Locate platelets.
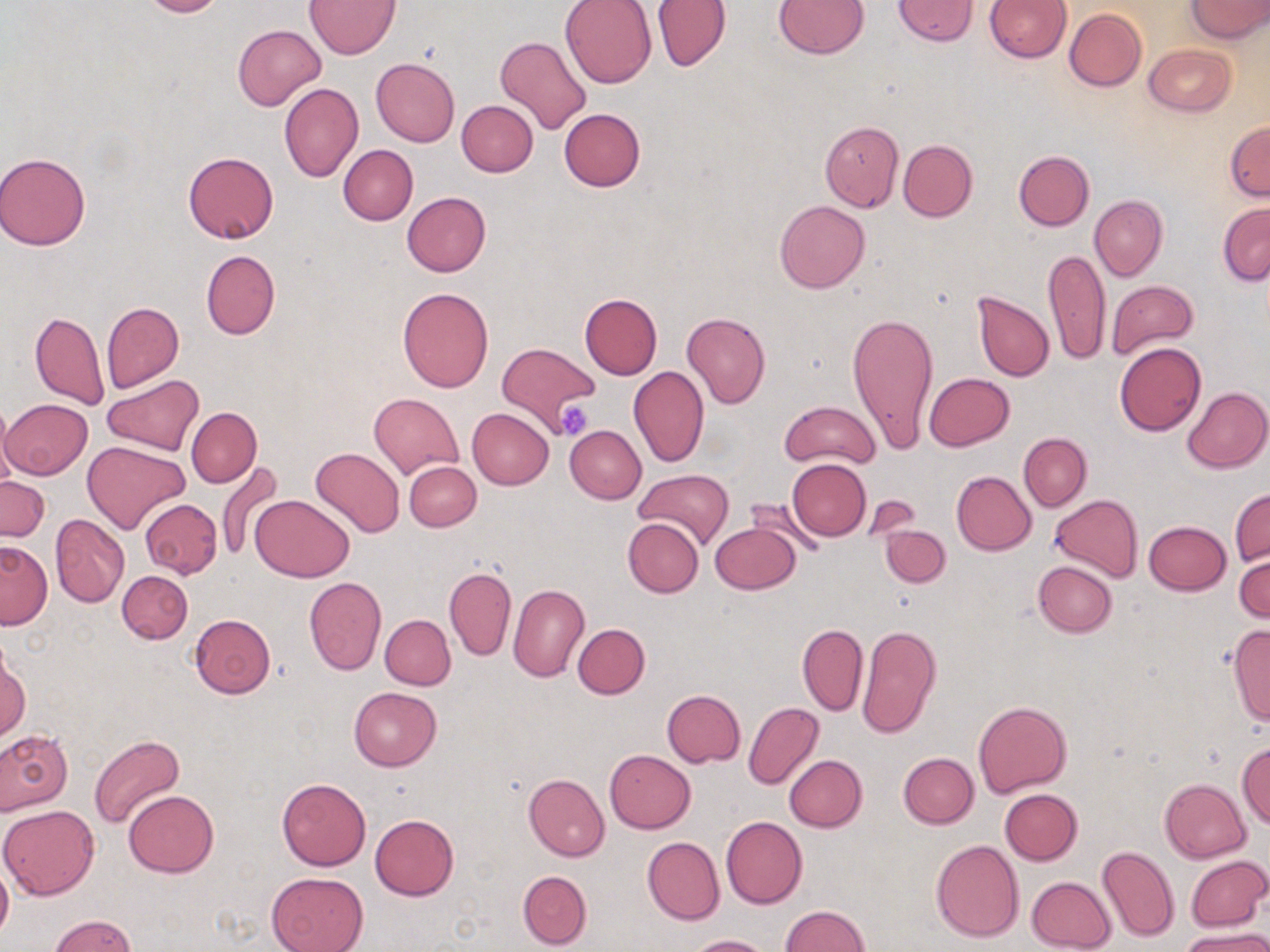
Approximate bounding boxes as (x1, y1, x2, y2) in pixels.
Platelets: (556, 400, 592, 441).

Uninfected red blood cell locations: (138, 0, 225, 18), (561, 0, 656, 88), (651, 0, 729, 71), (774, 0, 869, 58), (893, 0, 977, 44), (985, 0, 1070, 62), (1185, 0, 1268, 41), (304, 1, 401, 58), (1064, 8, 1146, 91), (234, 25, 326, 111), (494, 35, 592, 136), (1144, 42, 1236, 116), (371, 57, 460, 147), (278, 82, 364, 182), (456, 100, 538, 176), (559, 108, 646, 191), (820, 120, 904, 211), (1224, 121, 1270, 201), (898, 140, 977, 221), (338, 145, 418, 225), (1014, 150, 1094, 230), (183, 151, 278, 243), (0, 152, 92, 250), (402, 192, 491, 276), (1089, 194, 1167, 281), (774, 200, 870, 293), (1217, 202, 1270, 285), (1044, 247, 1110, 366), (201, 250, 280, 339), (1106, 279, 1199, 360), (398, 287, 494, 392), (972, 291, 1054, 381), (580, 292, 662, 379), (102, 302, 184, 393), (846, 310, 939, 454), (30, 311, 109, 410), (681, 312, 770, 409), (497, 341, 598, 433), (1114, 342, 1206, 436), (629, 366, 709, 468), (924, 372, 1015, 451), (101, 376, 204, 455), (1184, 386, 1268, 473), (369, 392, 463, 479), (0, 399, 91, 480), (780, 400, 881, 469), (0, 403, 17, 498), (467, 407, 553, 490), (187, 408, 261, 487), (565, 425, 646, 503), (1019, 432, 1092, 511), (83, 441, 189, 535), (311, 447, 405, 538), (787, 459, 871, 541), (215, 460, 286, 562), (404, 462, 480, 531), (634, 468, 734, 549), (952, 470, 1036, 554), (0, 475, 49, 541), (1230, 489, 1269, 567), (251, 495, 354, 582), (746, 495, 824, 558), (1050, 495, 1143, 581), (138, 498, 222, 578), (51, 514, 129, 608), (622, 519, 703, 598), (1144, 521, 1230, 596), (710, 522, 801, 594), (882, 524, 951, 587), (0, 541, 52, 629), (1235, 549, 1269, 624), (1033, 561, 1117, 637), (444, 567, 516, 661), (117, 571, 192, 644), (303, 576, 386, 675), (508, 585, 589, 682), (190, 613, 276, 697), (380, 615, 456, 690), (572, 623, 650, 699), (1228, 623, 1270, 728), (797, 624, 868, 716), (856, 624, 942, 739), (0, 651, 29, 742), (349, 687, 442, 770), (662, 689, 746, 767), (973, 701, 1071, 797), (744, 702, 823, 791), (0, 730, 72, 815), (88, 734, 185, 830), (1236, 742, 1270, 829), (605, 750, 696, 833), (899, 753, 979, 828), (784, 755, 867, 831), (523, 774, 609, 861), (277, 777, 371, 870), (1159, 778, 1252, 863), (999, 789, 1083, 864), (124, 790, 218, 878), (0, 804, 99, 900), (370, 814, 459, 900), (721, 815, 807, 909), (642, 837, 724, 925), (931, 840, 1024, 944), (1097, 845, 1180, 942), (1186, 855, 1268, 932), (0, 860, 12, 944), (518, 871, 592, 949), (265, 872, 368, 952), (1026, 876, 1117, 952), (780, 905, 870, 952), (51, 915, 136, 952), (1181, 929, 1270, 952), (687, 934, 773, 952). Slide-level diagnosis: negative for blood parasites. Captured at 1000x magnification. Thin blood smear. Optical microscopy. May-Grünwald-Giemsa stain. One field of a larger specimen. Image is 1270×952 pixels.